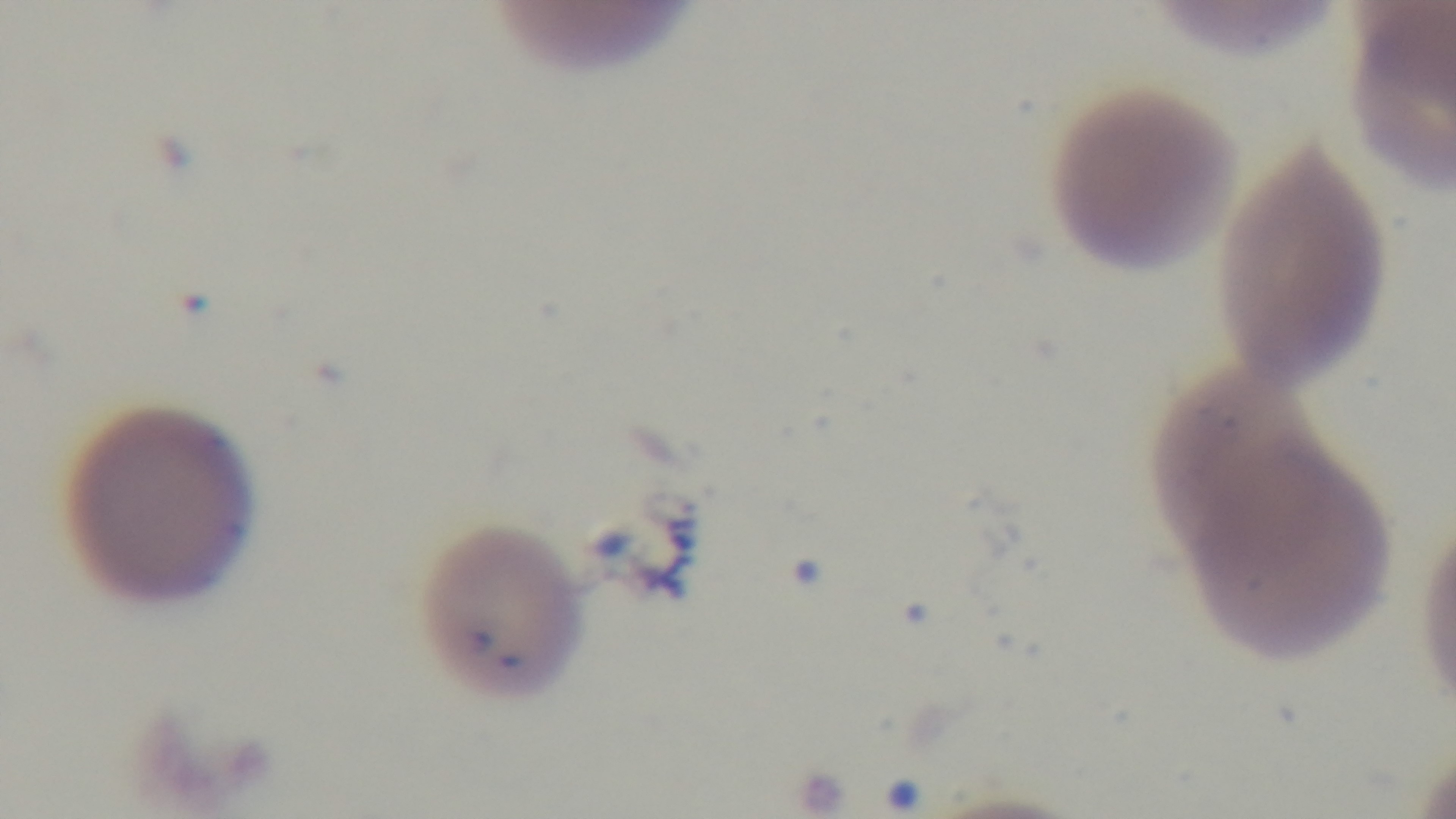

Summary:
  - Modality: light microscopy
  - Stain: Giemsa
  - Capture: mounted 4K digital camera
  - Preparation: thin
  - Field of view: one from the slide
  - Malaria status: infected
  - Objective: 100x oil immersion